Identify the parasite.
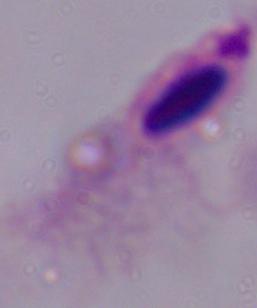

A trichomonad.

Micrograph. 1000x magnification.